Point out each leukocyte.
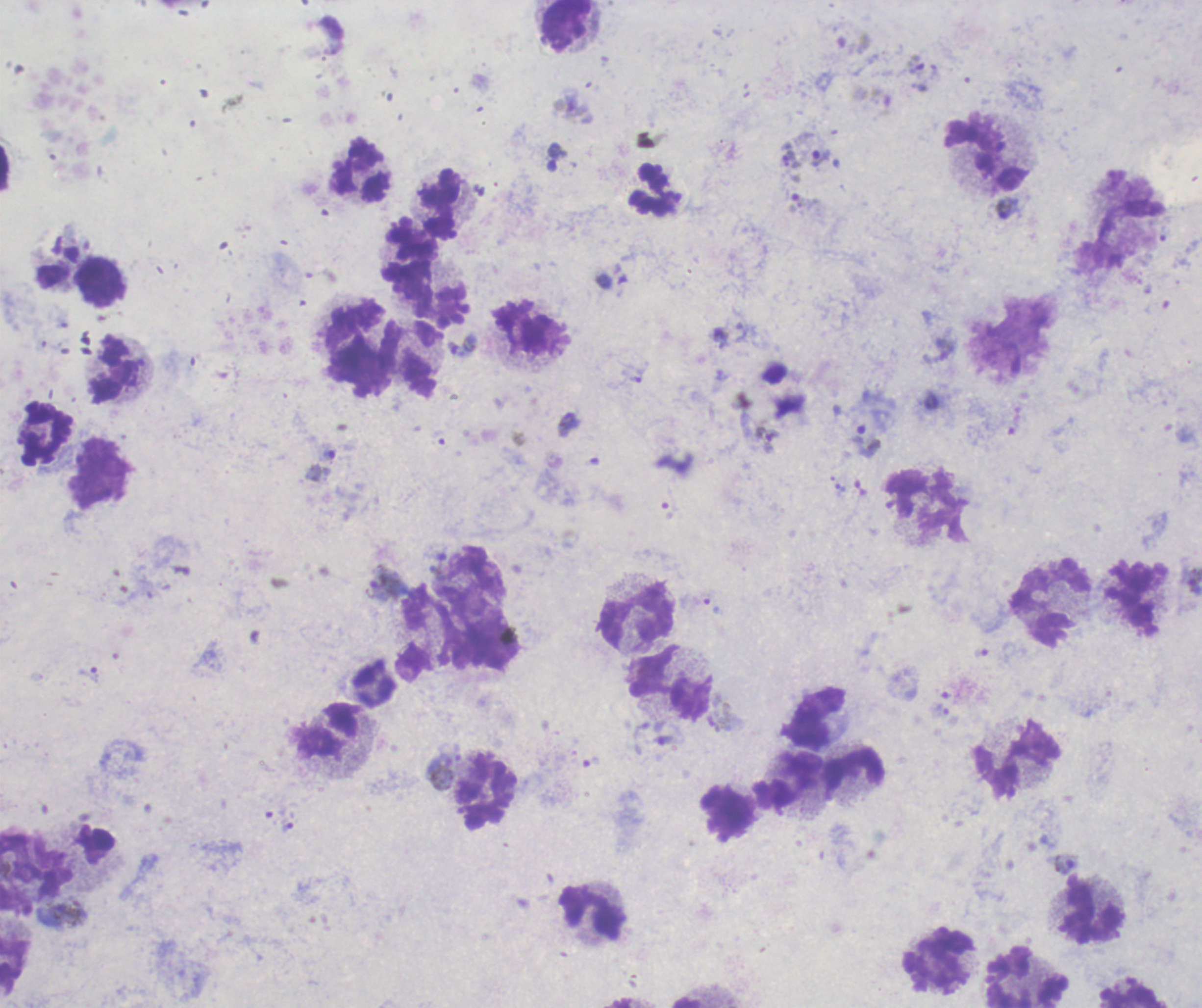
Approximate centers as [x, y] in pixels.
Leukocytes: [566, 25], [987, 154], [361, 174], [653, 190], [440, 205], [1118, 222], [411, 253], [100, 282], [428, 301], [352, 322], [528, 328], [410, 360], [361, 367], [115, 371], [47, 432], [100, 473], [927, 504], [1135, 598], [1050, 604], [636, 616], [671, 683], [374, 686], [817, 719], [328, 730], [1018, 758], [854, 770], [787, 780], [486, 791], [727, 812], [1091, 911], [593, 913], [937, 959], [14, 964], [1026, 978], [1133, 994].

Approximate centers as [x, y] in pixels. Trophozoite locations: [915, 64], [820, 157], [1007, 209], [939, 350], [767, 440], [866, 442], [330, 453], [1195, 582], [384, 585], [88, 674], [287, 825], [1066, 863]. Gametocyte locations: [570, 105]. Life-cycle stages observed: trophozoite, gametocyte. One field from this slide. Image is 1202×1008 pixels. Previously used in an actual diagnosis. Thick blood smear. Background quality: unsatisfactory. Result: positive for malaria parasites. 100x magnification. Romanowsky-stained preparation.